Locate every Plasmodium parasite.
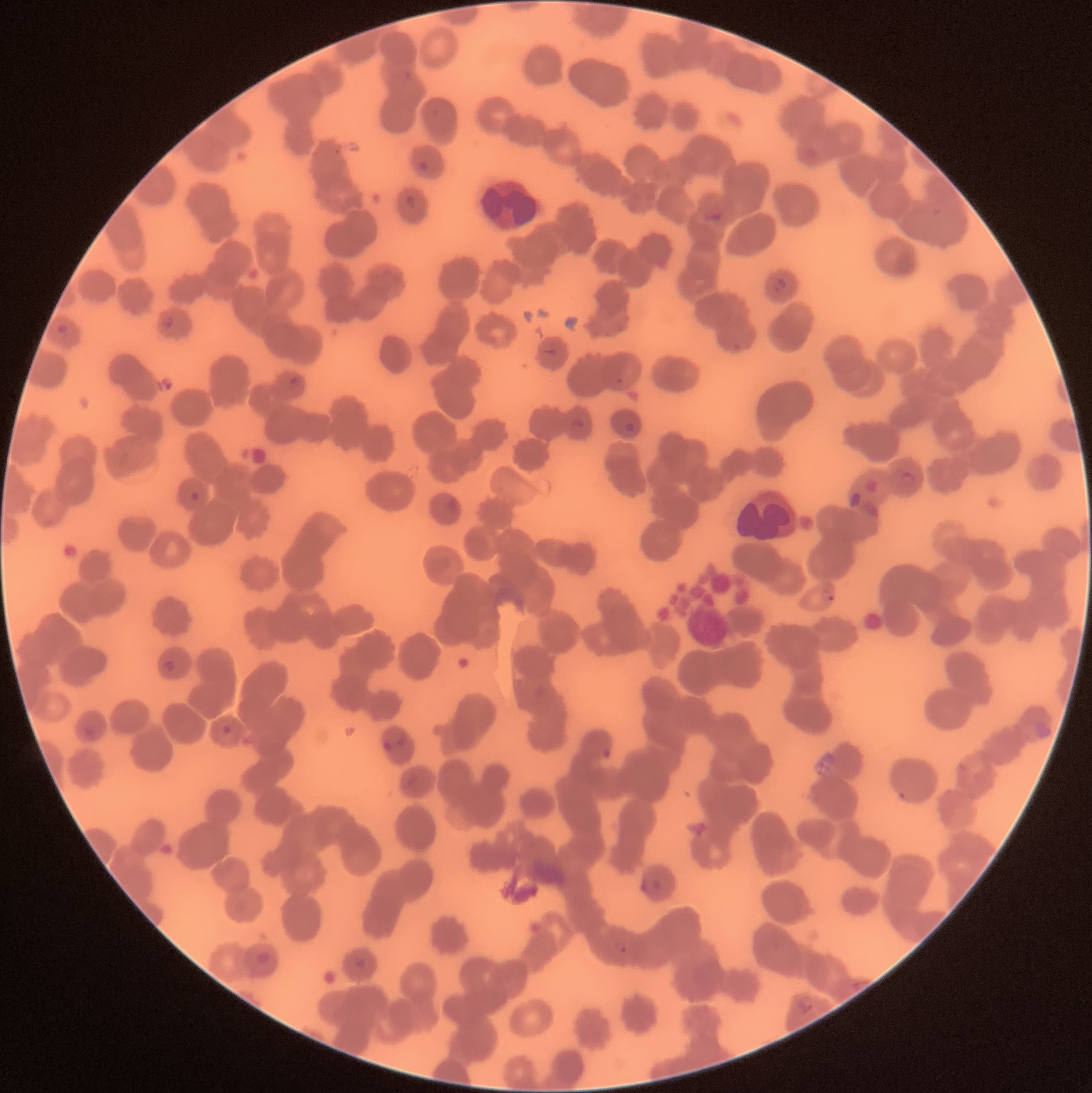
Approximate bounding boxes as [x1, y1, x2, y2] in pixels.
Plasmodium parasites: [417, 160, 429, 174], [405, 194, 417, 209], [773, 276, 787, 293], [160, 316, 174, 329], [287, 375, 304, 391], [625, 422, 636, 433], [899, 469, 917, 487], [190, 490, 200, 501], [821, 589, 834, 603], [163, 659, 175, 672], [222, 724, 232, 734], [381, 729, 406, 750], [603, 746, 612, 759], [640, 878, 662, 891], [618, 945, 628, 954], [254, 951, 271, 965], [353, 957, 367, 968], [795, 993, 818, 1014].

White blood cell locations: [479, 176, 543, 231], [735, 488, 799, 547]. The red blood cells show rouleaux formation. Thin blood smear. Optical microscopy. Image is 1092×1093 pixels.